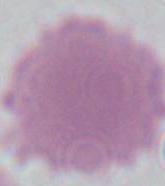
Summary:
  - Magnification: 1000x
  - Identification: erythrocyte
  - Modality: micrograph